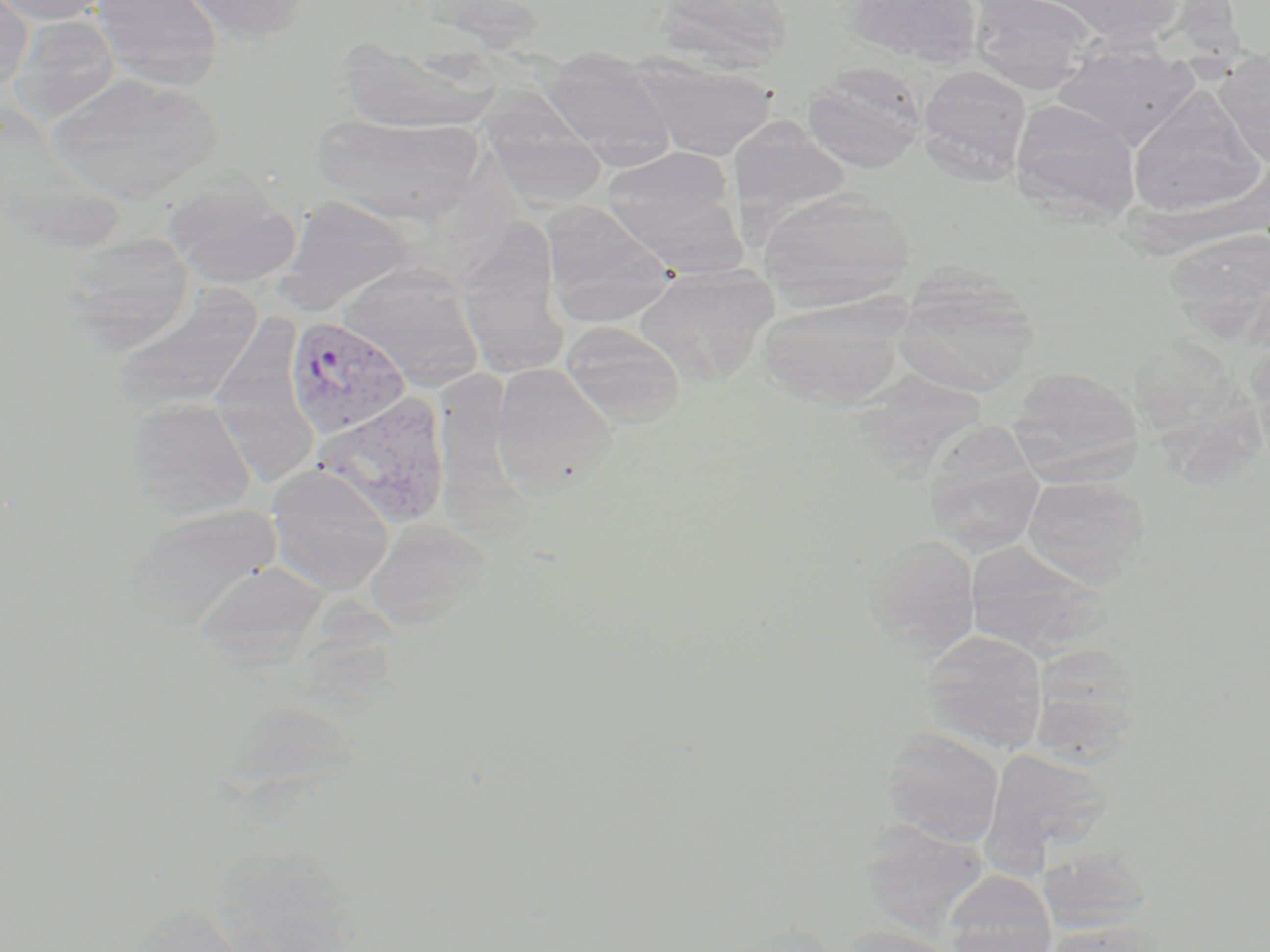
Summary:
  - Coordinate format: approximate bounding boxes as [x1, y1, x2, y2] in pixels
  - Uninfected red blood cell locations: [0, 0, 113, 26], [91, 0, 224, 90], [173, 0, 315, 45], [652, 0, 793, 71], [845, 0, 984, 69], [1052, 0, 1189, 46], [0, 1, 33, 93], [968, 1, 1097, 92], [13, 15, 120, 123], [334, 36, 498, 133], [1052, 41, 1200, 147], [540, 47, 677, 166], [1215, 49, 1270, 168], [631, 55, 778, 159], [803, 61, 927, 173], [917, 65, 1032, 184], [44, 71, 224, 204], [1127, 87, 1266, 218], [1009, 98, 1142, 221], [482, 99, 608, 212], [311, 113, 484, 225], [728, 119, 848, 228], [601, 147, 738, 262], [162, 172, 302, 289], [756, 188, 917, 312], [274, 195, 415, 317], [538, 201, 676, 325], [457, 225, 570, 379], [1162, 229, 1270, 335], [61, 233, 197, 348], [340, 265, 484, 389], [634, 265, 779, 387], [893, 276, 1040, 399], [109, 285, 263, 416], [757, 296, 909, 410], [560, 321, 687, 428], [1130, 331, 1264, 489], [489, 363, 620, 500], [1006, 366, 1144, 479], [860, 371, 992, 476], [126, 396, 257, 520], [935, 419, 1049, 554], [266, 464, 396, 596], [1021, 475, 1151, 587], [122, 502, 282, 633], [366, 517, 493, 631], [861, 533, 981, 657], [963, 542, 1110, 660], [191, 559, 329, 666], [918, 629, 1049, 754], [1027, 643, 1146, 763], [879, 727, 1005, 848], [981, 748, 1115, 870], [857, 822, 991, 938], [1038, 847, 1154, 934], [942, 871, 1057, 952], [1039, 922, 1168, 952], [836, 925, 964, 952]
  - Plasmodium vivax-infected red blood cell locations: [284, 314, 412, 439], [308, 393, 453, 533]
  - Slide-level diagnosis: Plasmodium vivax
  - Stain: May-Grünwald-Giemsa
  - Magnification: 1000x
  - Image size: 1270×952 pixels
  - Field of view: one of a larger specimen
  - Modality: light microscopy
  - Preparation: thin blood film